Assess the morphology of the red blood cells.
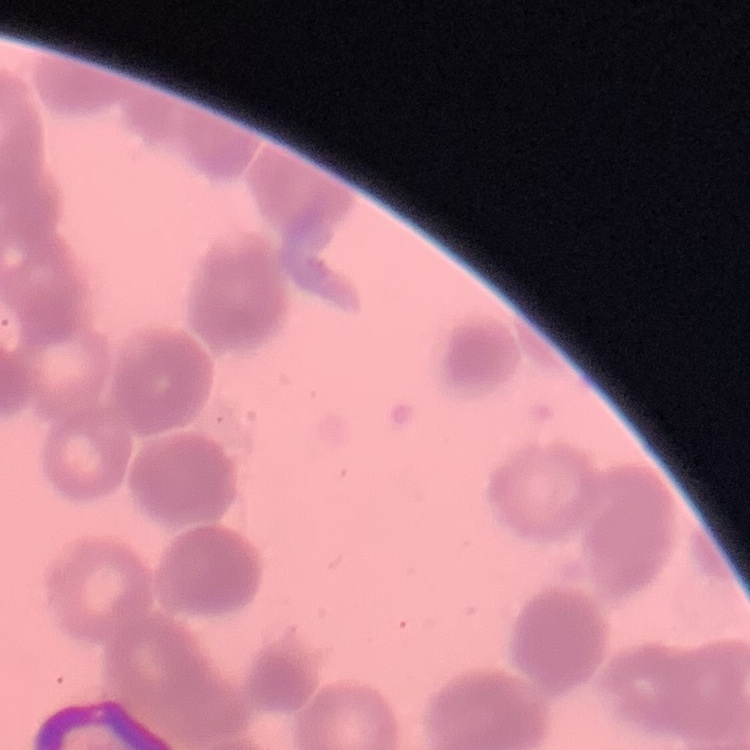
Rouleaux formation.

Summary:
  - Image type: one tile cut from a larger photomicrograph
  - Preparation: thin blood smear
  - Stain: Field's or Giemsa